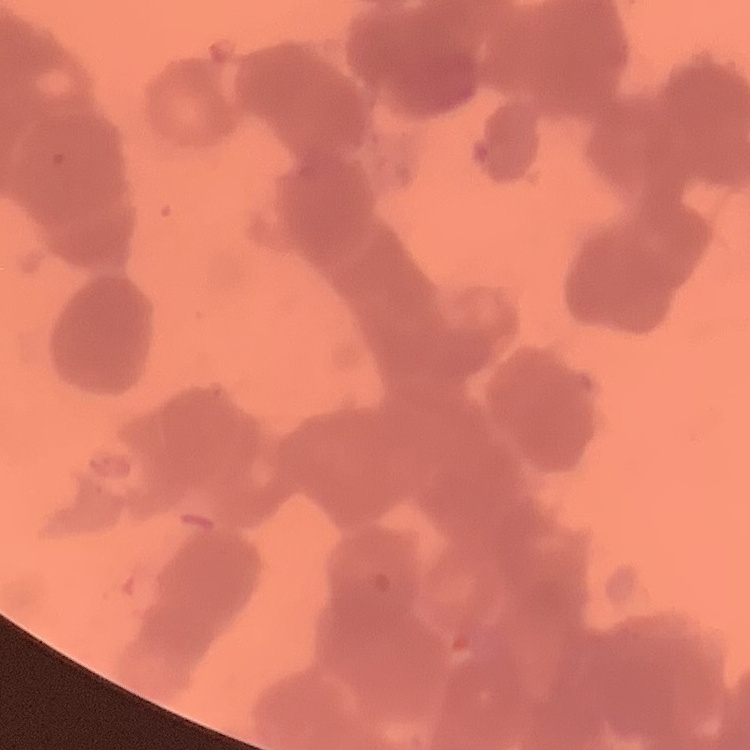
The red blood cells show rouleaux formation. Square crop of a larger photomicrograph. Thin peripheral smear. Field's or Giemsa stain.